Locate and identify every blood parasite.
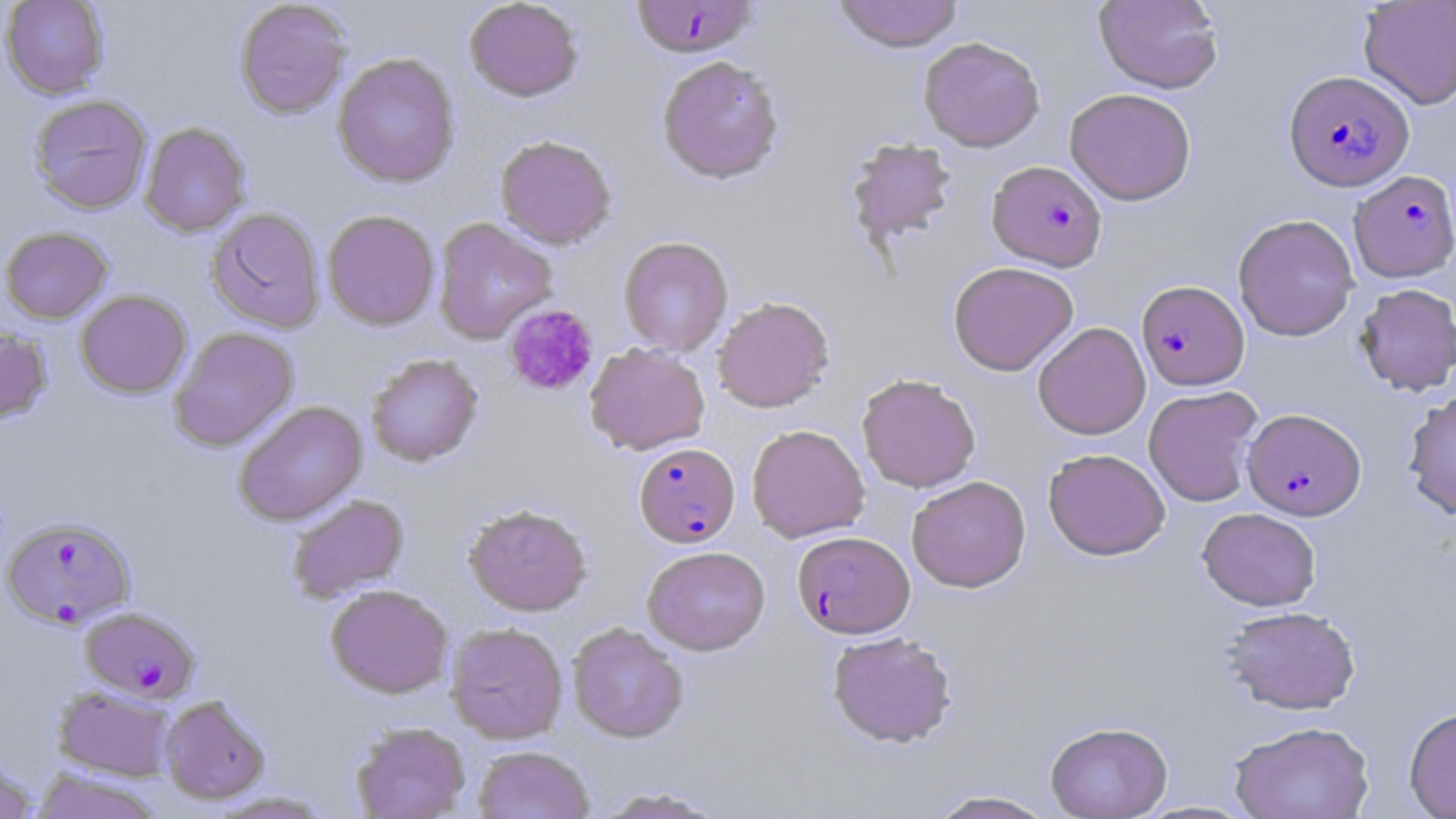
Approximate bounding boxes as (x1, y1, x2, y2) in pixels.
Plasmodium falciparum-infected red blood cells: (630, 0, 760, 58), (1283, 70, 1413, 190), (987, 160, 1107, 271), (1349, 170, 1456, 282), (1136, 280, 1249, 390), (1242, 407, 1366, 521), (634, 443, 739, 547), (2, 517, 136, 629), (792, 531, 915, 638), (80, 606, 201, 703).
No Plasmodium ovale, Plasmodium malariae, Plasmodium vivax, Babesia divergens, or Trypanosoma brucei observed.

Summary:
  - Platelet locations: (503, 304, 599, 397)
  - Uninfected red blood cell locations: (0, 0, 109, 99), (234, 0, 352, 119), (464, 0, 583, 102), (832, 0, 964, 53), (1093, 0, 1224, 94), (1358, 0, 1456, 110), (918, 36, 1045, 152), (333, 53, 461, 188), (656, 55, 785, 185), (1065, 88, 1196, 205), (28, 94, 153, 215), (140, 121, 251, 237), (495, 134, 617, 249), (845, 137, 958, 247), (206, 207, 325, 333), (322, 209, 440, 331), (1233, 213, 1360, 341), (432, 217, 558, 344), (0, 226, 113, 324), (618, 236, 733, 357), (948, 261, 1079, 376), (1354, 283, 1456, 396), (75, 290, 192, 398), (712, 296, 835, 413), (1032, 322, 1151, 440), (0, 327, 53, 425), (170, 327, 299, 451), (584, 343, 711, 455), (366, 353, 483, 467), (857, 373, 980, 492), (1143, 385, 1264, 507), (1402, 388, 1456, 520), (233, 400, 368, 526), (746, 424, 870, 543), (1043, 448, 1170, 560), (907, 475, 1031, 592), (287, 494, 409, 602), (463, 502, 592, 616), (1198, 507, 1321, 611), (642, 546, 770, 655), (325, 584, 453, 698), (1221, 605, 1361, 715), (446, 622, 569, 744), (567, 622, 688, 743), (827, 631, 957, 748), (53, 685, 177, 782), (159, 694, 270, 804), (1404, 705, 1456, 818), (1045, 720, 1173, 818), (1228, 720, 1375, 819), (350, 721, 470, 819), (473, 745, 595, 819), (0, 753, 39, 819), (31, 768, 163, 819), (592, 786, 730, 818), (927, 789, 1059, 818), (210, 790, 335, 817), (1135, 800, 1259, 818)
  - Slide-level diagnosis: Plasmodium falciparum
  - Magnification: 1000x
  - Field of view: one of a larger specimen
  - Modality: optical microscopy
  - Preparation: thin blood film
  - Stain: May-Grünwald-Giemsa
  - Image size: 1456×819 pixels